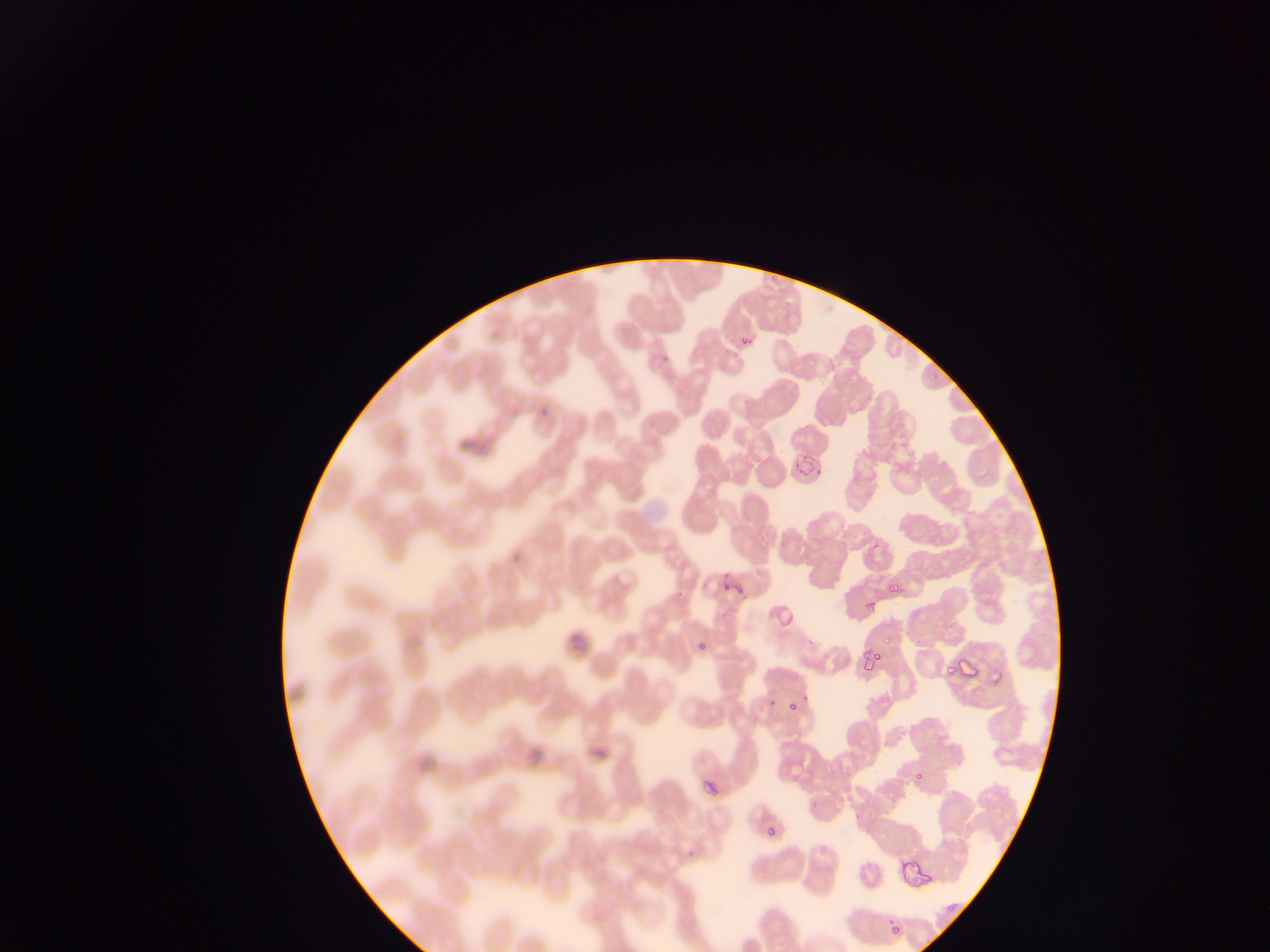

Approximate bounding boxes as (left, top, right, bottom) in pixels. Plasmodium parasite locations: (795, 457, 819, 477), (869, 538, 885, 558), (887, 574, 905, 589), (719, 580, 747, 595), (863, 600, 892, 612), (700, 636, 712, 653), (861, 657, 886, 669), (939, 665, 959, 676), (764, 678, 785, 708), (788, 698, 809, 713), (695, 756, 743, 797), (911, 760, 939, 790), (761, 819, 791, 838), (888, 921, 902, 939). Thin blood film. Collected in Ghana. Mobile-phone photograph taken through the microscope. Image is 1270×952 pixels. Single field of view.